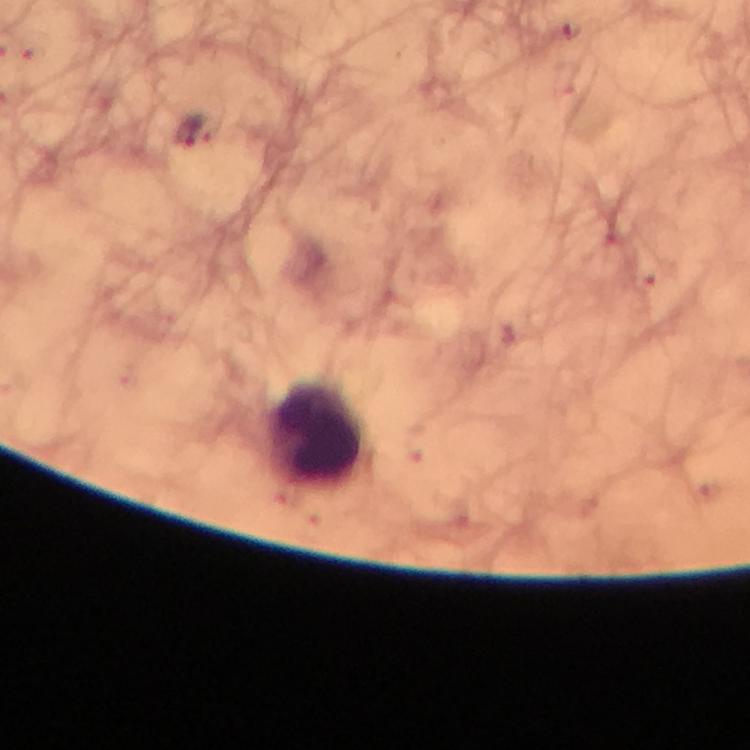 Approximate object centers, in pixels from the top-left corner. Plasmodium parasite locations: (x=187, y=132). Leukocyte locations: (x=321, y=435). Immersion oil applied. Smartphone photograph taken through a microscope. Image is 750×750 pixels. 100x magnification. A crop from one field of view. From a diagnostic examination for malaria. Thick blood smear. Giemsa stain.